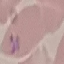

Result: malaria parasites detected. Thin smear of blood. Cell patch, automatically extracted from a larger field of view and resized to 64 × 64 pixels. Acquired by smartphone through the microscope eyepiece. Giemsa-stained preparation.